Identify the parasite.
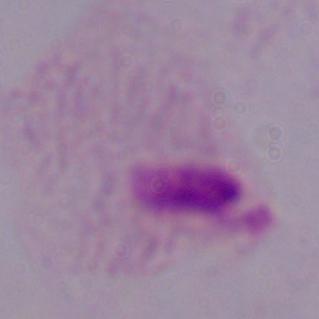

A trichomonad.

magnification = 1000x
modality = photomicrograph